Locate and identify every blood parasite.
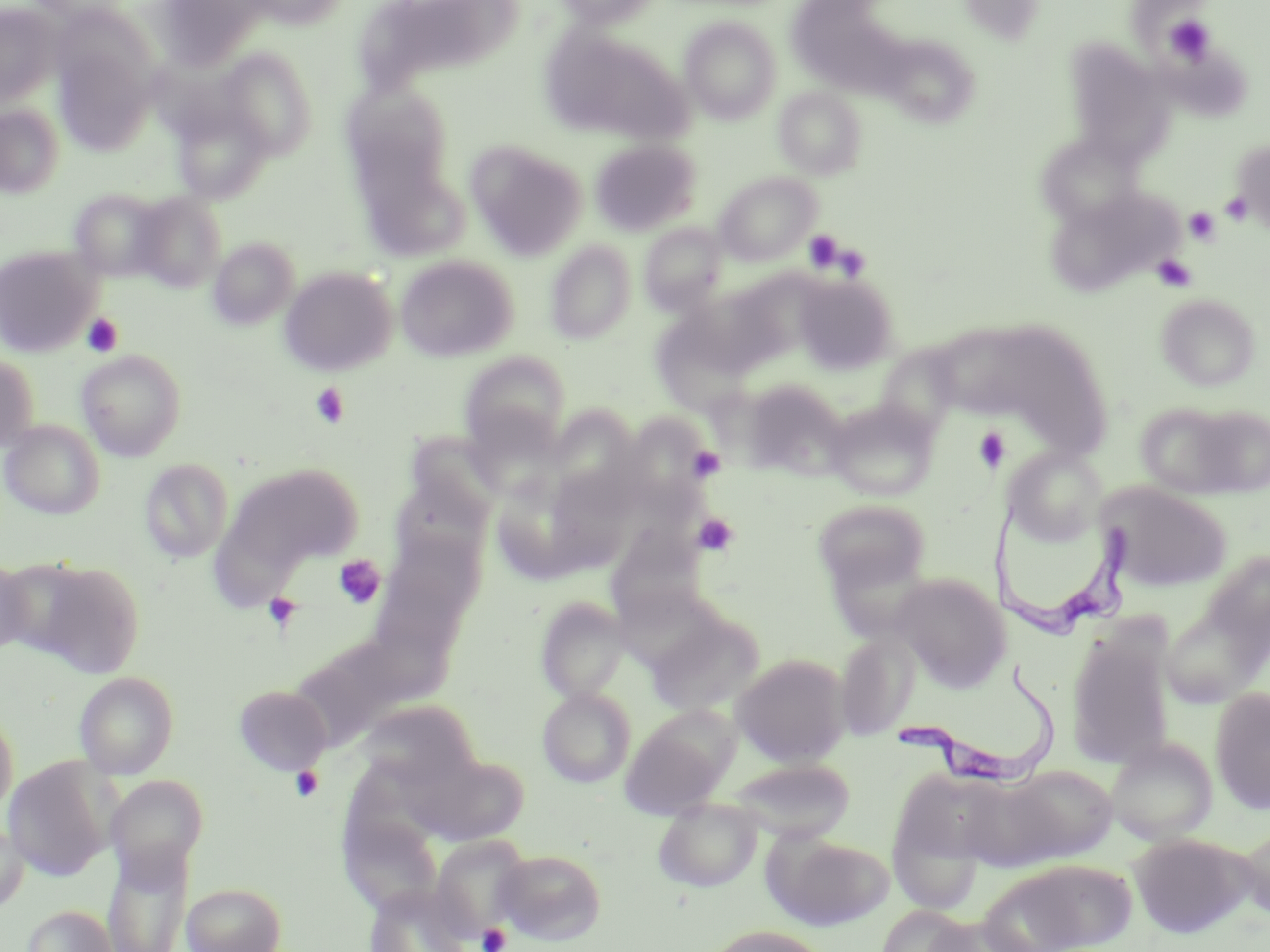
Approximate bounding boxes as (x1, y1, x2, y2) in pixels.
Trypanosoma brucei: (990, 499, 1139, 640), (895, 665, 1065, 789).
No Plasmodium falciparum, Plasmodium ovale, Plasmodium malariae, Plasmodium vivax, or Babesia divergens observed.

Platelet locations: (1163, 14, 1217, 65), (1220, 191, 1253, 225), (1184, 206, 1221, 245), (803, 229, 845, 270), (1152, 254, 1197, 292), (82, 313, 123, 356), (310, 382, 350, 429), (973, 427, 1012, 473), (687, 445, 725, 481), (692, 513, 739, 556), (334, 555, 385, 608), (262, 592, 303, 633), (290, 766, 324, 802), (477, 923, 511, 952). Uninfected red blood cell locations: (152, 0, 275, 71), (550, 0, 664, 28), (795, 0, 879, 83), (957, 0, 1047, 45), (0, 2, 63, 106), (680, 17, 782, 125), (538, 26, 695, 149), (874, 32, 982, 129), (53, 33, 160, 154), (1063, 40, 1176, 164), (216, 48, 318, 159), (340, 82, 463, 200), (773, 87, 867, 180), (171, 98, 275, 203), (0, 103, 64, 198), (1230, 138, 1270, 234), (590, 139, 701, 236), (466, 140, 588, 260), (1039, 146, 1145, 229), (355, 155, 470, 262), (714, 171, 821, 266), (1046, 186, 1183, 297), (69, 188, 172, 282), (132, 192, 227, 292), (640, 223, 729, 315), (208, 236, 299, 329), (545, 240, 636, 344), (0, 245, 100, 356), (394, 254, 518, 361), (279, 265, 397, 376), (793, 272, 898, 374), (689, 281, 802, 381), (1156, 293, 1260, 391), (933, 321, 1045, 419), (660, 322, 753, 422), (1011, 335, 1113, 458), (875, 343, 964, 438), (76, 348, 187, 461), (459, 350, 571, 455), (0, 352, 40, 453), (739, 377, 850, 479), (826, 399, 941, 500), (1133, 401, 1255, 499), (550, 407, 644, 507), (0, 419, 105, 519), (406, 431, 506, 527), (1005, 446, 1107, 546), (138, 458, 234, 563), (225, 462, 363, 572), (495, 467, 598, 579), (389, 476, 490, 568), (1094, 481, 1232, 592), (813, 498, 931, 597), (214, 517, 302, 614), (604, 527, 706, 631), (391, 540, 491, 631), (1200, 547, 1269, 667), (0, 556, 32, 656), (835, 557, 931, 648), (30, 561, 145, 678), (890, 573, 1012, 690), (535, 596, 630, 703), (1160, 603, 1265, 708), (646, 611, 764, 717), (365, 619, 461, 708), (1066, 626, 1175, 769), (836, 631, 920, 739), (292, 651, 395, 745), (731, 653, 851, 766), (75, 671, 179, 778), (233, 685, 332, 775), (537, 687, 635, 787), (1210, 687, 1270, 814), (360, 699, 482, 790), (0, 705, 19, 816), (619, 708, 736, 818), (1105, 737, 1218, 845), (416, 751, 530, 844), (3, 758, 113, 880), (729, 758, 855, 842), (1001, 764, 1118, 863), (887, 767, 1006, 906), (104, 774, 208, 882), (653, 797, 764, 892), (0, 818, 29, 913), (340, 823, 441, 926), (1235, 826, 1270, 922), (764, 832, 895, 930), (429, 834, 530, 942), (1129, 834, 1252, 938), (103, 841, 194, 952), (494, 849, 607, 944), (987, 859, 1137, 951), (181, 881, 287, 952), (365, 883, 472, 952), (22, 904, 118, 952), (877, 904, 975, 952), (923, 915, 1034, 952), (703, 925, 833, 952). Slide-level diagnosis: Trypanosoma brucei. Thin blood smear. Captured at 1000x magnification. Image is 1270×952 pixels. Single field of view. May-Grünwald-Giemsa-stained preparation. Optical microscopy.